Report the malaria status of this cell.
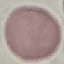
Uninfected.

capture = smartphone camera at the microscope eyepiece
image type = cell patch, automatically extracted from a larger field of view and resized to 64 × 64 pixels
preparation = thin blood film
stain = Giemsa